Identify the preparation type.
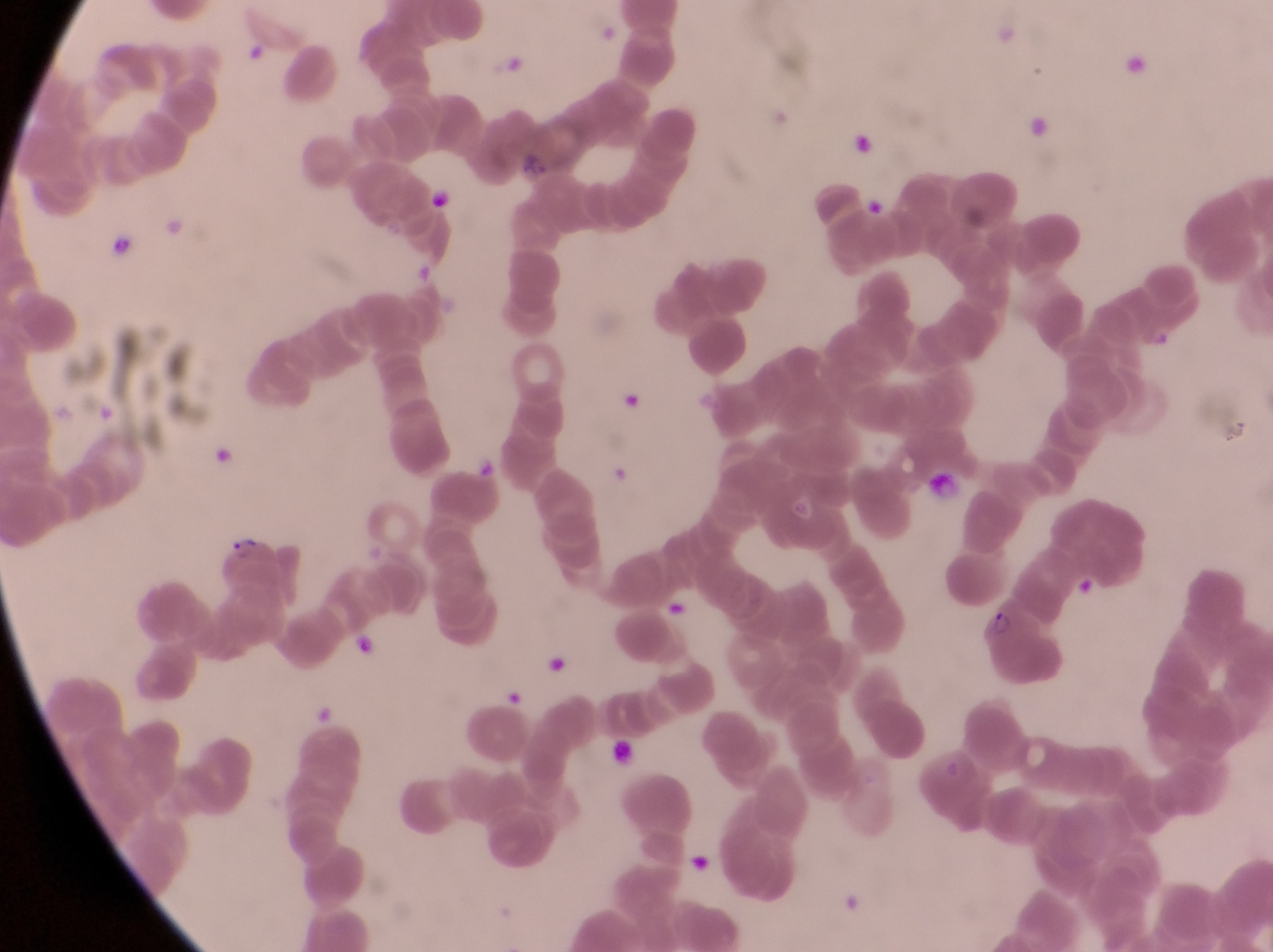
This is a thin smear.

Approximate bounding boxes as {left, top, right, bottom} in pixels. Parasitised red blood cell locations: {225, 530, 270, 569}, {984, 604, 1071, 689}. Artifact (platelet-like body, stain precipitate, or debris) locations: {245, 42, 269, 68}, {1128, 50, 1149, 77}, {1020, 112, 1054, 146}, {850, 132, 879, 163}, {427, 186, 458, 217}, {108, 233, 136, 262}, {474, 453, 498, 477}, {1079, 575, 1103, 599}, {354, 633, 377, 660}, {549, 651, 572, 679}, {505, 688, 528, 715}, {608, 739, 641, 775}. Image is 1273×952 pixels. Captured by a smartphone held over the eyepiece of an Olympus CX-23 microscope. Collected in Uganda. At a magnification of 1000x. Single field of view.